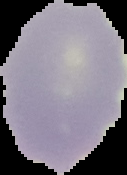
From a thin blood smear. Image is 127×175 pixels. Cell region segmented out of the field of view; the surrounding area is masked to black. Malaria status: uninfected.